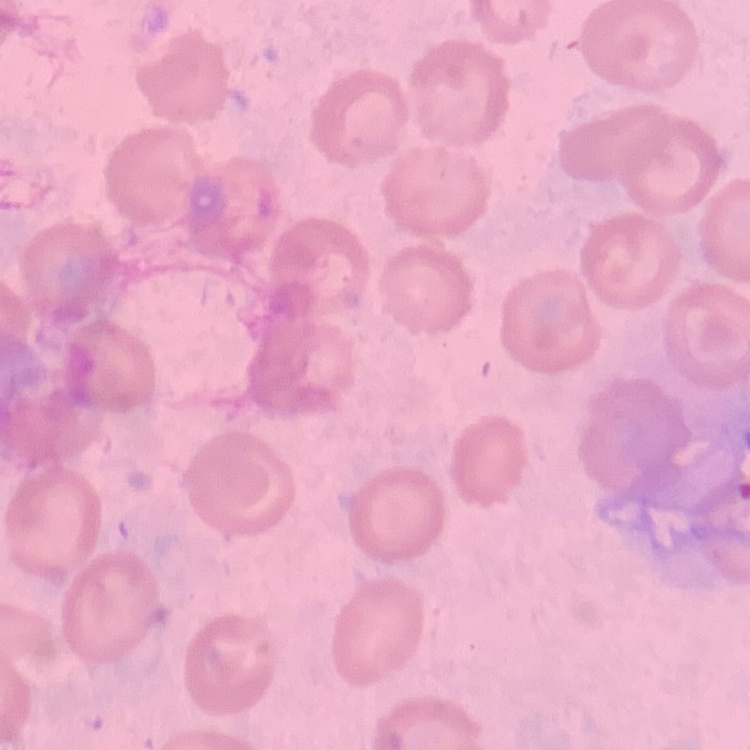
The red blood cells show no rouleaux formation. Thin peripheral smear. Field's or Giemsa stain. Square crop of a larger photomicrograph.